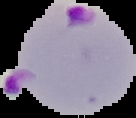
Summary:
  - Result: malaria parasites identified
  - Image size: 136×118 pixels
  - Preparation: thin blood film
  - Image type: cell region segmented out of the field of view; surrounding area masked to black